Classify this cell by malaria status.
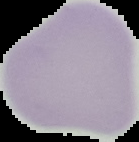

It is uninfected.

Image is 139×142 pixels. Segmented cell region on a black background. From a thin blood smear.